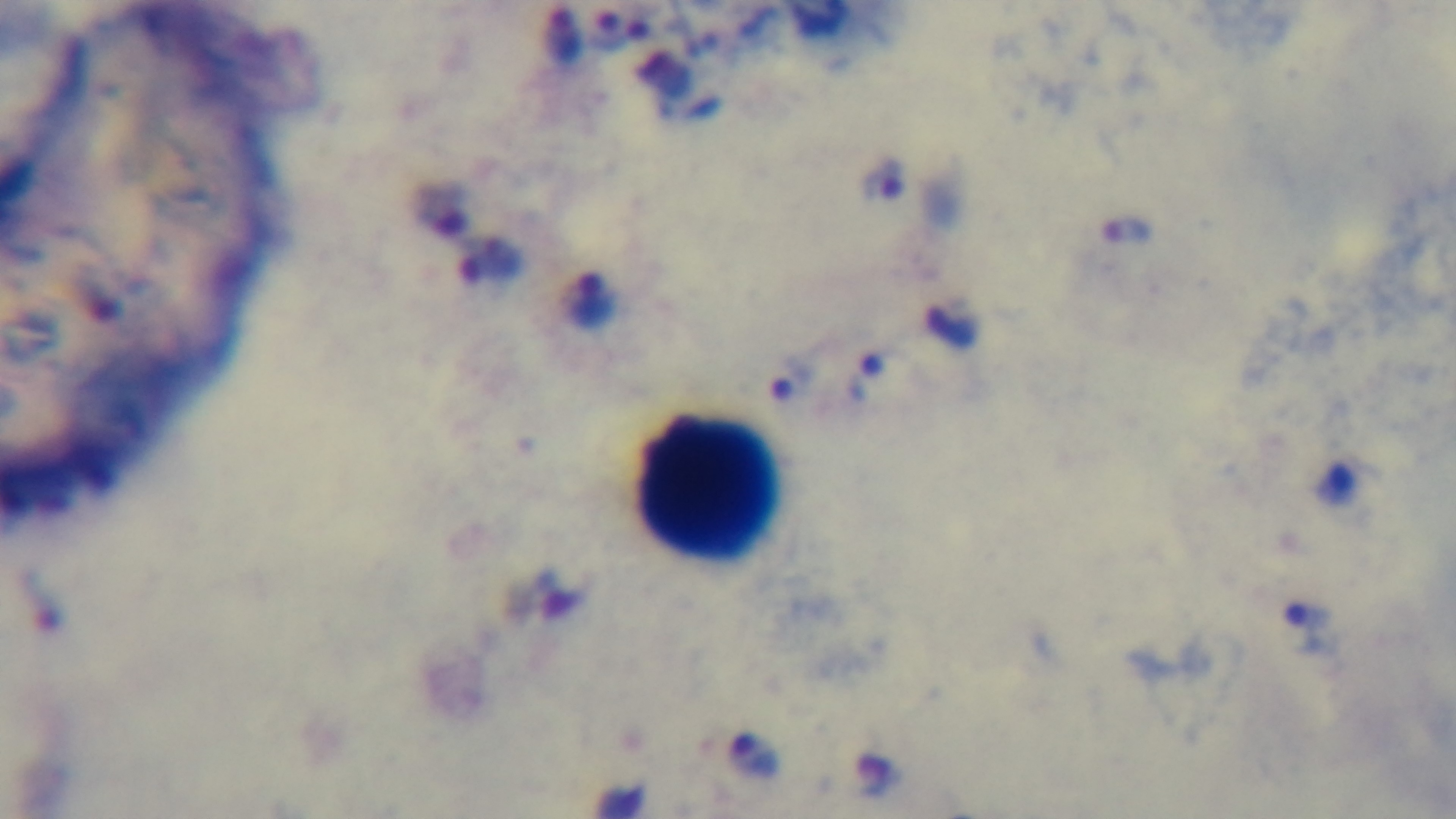

Summary:
  - Modality: light microscopy
  - Malaria status: infected
  - Capture: mounted 4K digital camera
  - Stain: Giemsa
  - Objective: 100x oil immersion
  - Field of view: one from the slide
  - Preparation: thick blood film